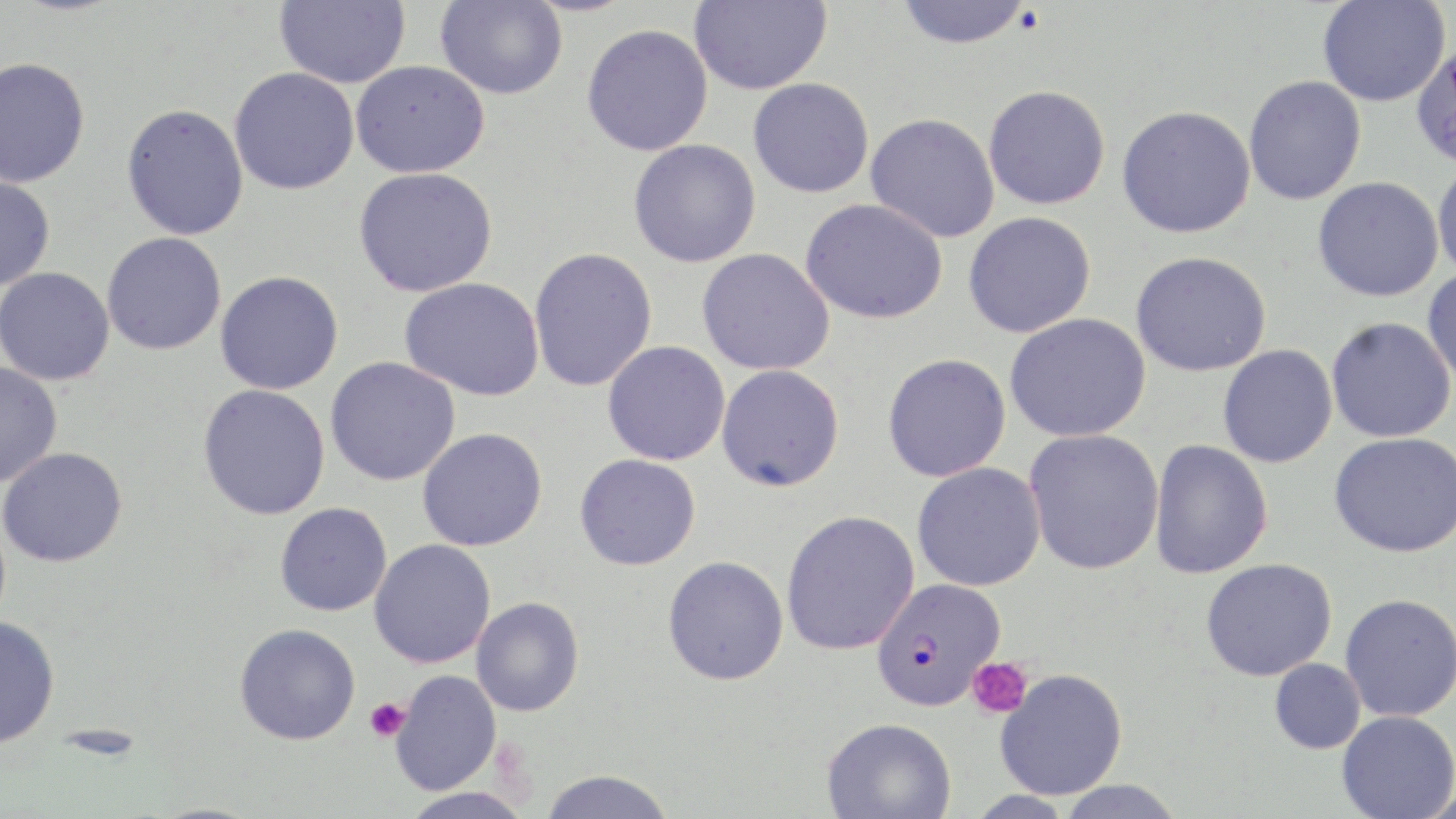
{
  "slide_level_diagnosis": "Plasmodium falciparum",
  "modality": "light microscopy",
  "image_size": "1456×819 pixels",
  "platelet_locations": "approximate bounding boxes as (x1,y1)-(x2,y2) corner pairs in pixels: (966,657)-(1032,719), (365,698)-(409,742)",
  "plasmodium_falciparum_infected_red_blood_cell_locations": "approximate bounding boxes as (x1,y1)-(x2,y2) corner pairs in pixels: (871,577)-(1006,709)",
  "field_of_view": "single",
  "preparation": "thin blood smear",
  "stain": "May-Grünwald-Giemsa",
  "uninfected_red_blood_cell_locations": "approximate bounding boxes as (x1,y1)-(x2,y2) corner pairs in pixels: (274,0)-(410,88), (436,0)-(567,99), (690,0)-(831,95), (895,0)-(1033,48), (1318,0)-(1450,106), (581,23)-(713,156), (1409,44)-(1456,167), (0,57)-(91,188), (351,60)-(489,177), (229,67)-(359,195), (1244,75)-(1366,205), (748,77)-(874,198), (983,84)-(1111,210), (121,102)-(249,241), (1117,105)-(1256,238), (865,113)-(1001,242), (628,139)-(761,268), (1432,157)-(1456,283), (353,167)-(498,297), (0,174)-(56,291), (1311,176)-(1445,302), (800,198)-(948,323), (963,211)-(1096,338), (101,232)-(227,355), (528,247)-(657,392), (697,248)-(834,376), (1131,251)-(1272,377), (1422,266)-(1456,388), (0,267)-(115,386), (215,271)-(344,395), (399,277)-(545,401), (1005,313)-(1151,442), (1326,316)-(1456,443), (603,341)-(730,466), (1217,344)-(1338,468), (882,353)-(1011,482), (325,357)-(461,486), (0,362)-(63,487), (716,364)-(844,492), (197,384)-(331,521), (417,427)-(548,551), (1024,428)-(1164,575), (1328,431)-(1456,558), (1149,439)-(1273,579), (0,447)-(127,567), (575,454)-(701,570), (912,462)-(1045,592), (275,502)-(392,616), (781,510)-(920,656), (369,539)-(496,668), (662,555)-(789,685), (1200,557)-(1337,682), (1339,593)-(1456,722), (471,597)-(584,717), (0,616)-(60,748), (234,623)-(360,745), (1268,658)-(1366,754), (994,668)-(1128,800), (391,670)-(501,794), (1336,710)-(1456,819), (822,717)-(956,819), (537,769)-(676,818), (1053,780)-(1188,819), (397,786)-(536,818), (964,790)-(1081,817)",
  "magnification": "1000x"
}